Locate and identify every blood parasite.
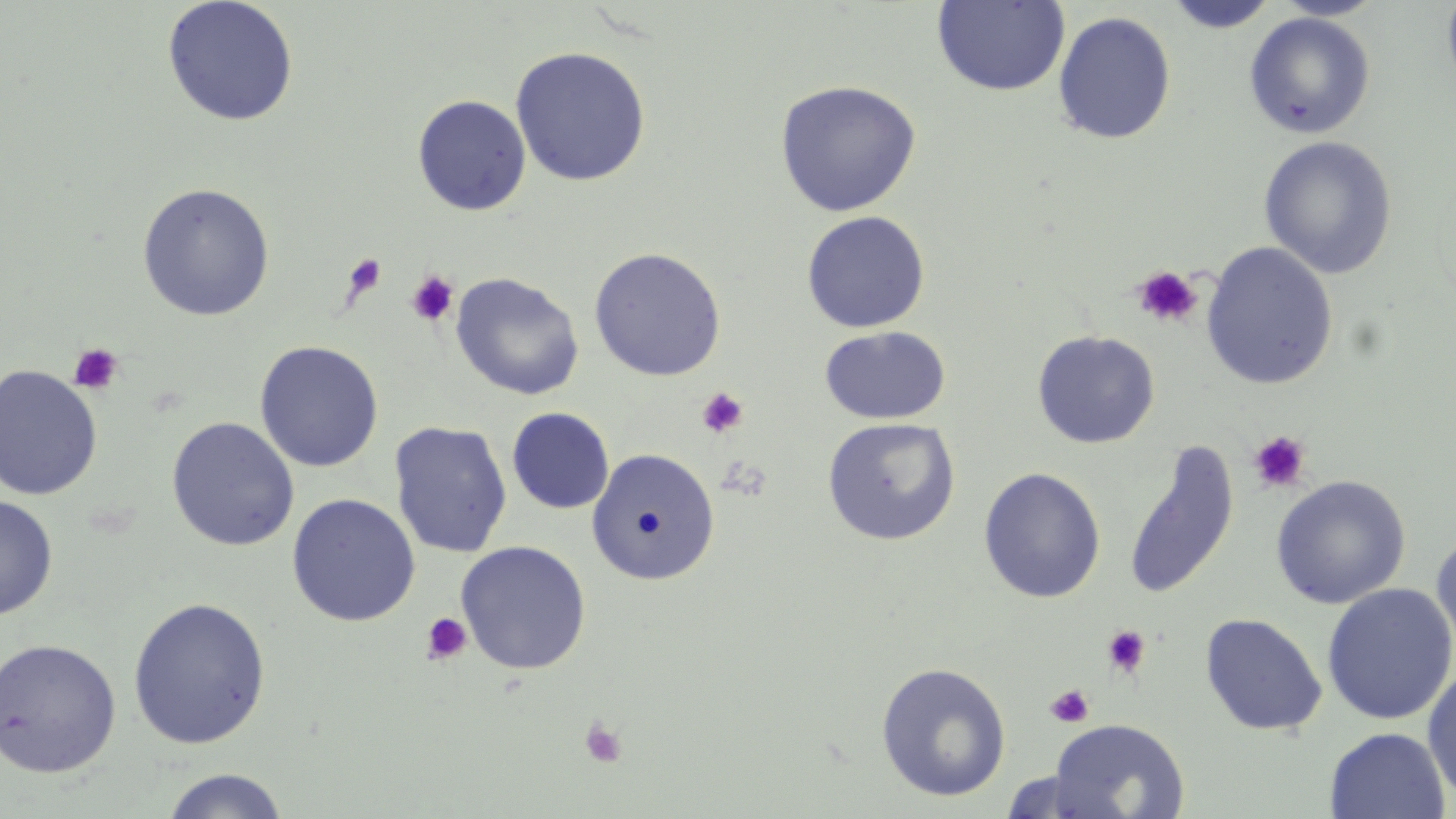
No blood parasites observed.

slide-level diagnosis = no evidence of blood parasites
image size = 1456×819 pixels
magnification = 1000x
field of view = single
platelet locations = approximate bounding boxes as named x1/y1/x2/y2 corners in pixels: (x1=342, y1=254, x2=388, y2=300), (x1=1132, y1=265, x2=1202, y2=328), (x1=406, y1=270, x2=459, y2=327), (x1=68, y1=343, x2=124, y2=396), (x1=696, y1=386, x2=749, y2=439), (x1=1249, y1=431, x2=1311, y2=493), (x1=420, y1=611, x2=473, y2=665), (x1=1101, y1=625, x2=1151, y2=679), (x1=1045, y1=684, x2=1094, y2=728), (x1=578, y1=716, x2=628, y2=769)
uninfected red blood cell locations = approximate bounding boxes as named x1/y1/x2/y2 corners in pixels: (x1=162, y1=0, x2=300, y2=127), (x1=1272, y1=0, x2=1387, y2=20), (x1=1441, y1=0, x2=1456, y2=101), (x1=931, y1=1, x2=1070, y2=96), (x1=1163, y1=1, x2=1279, y2=33), (x1=1053, y1=11, x2=1176, y2=145), (x1=1244, y1=12, x2=1375, y2=139), (x1=510, y1=45, x2=651, y2=186), (x1=774, y1=80, x2=922, y2=217), (x1=412, y1=94, x2=532, y2=216), (x1=1258, y1=135, x2=1398, y2=279), (x1=136, y1=183, x2=275, y2=321), (x1=801, y1=210, x2=930, y2=334), (x1=1201, y1=241, x2=1339, y2=390), (x1=588, y1=247, x2=727, y2=381), (x1=450, y1=273, x2=584, y2=400), (x1=819, y1=326, x2=951, y2=424), (x1=1032, y1=330, x2=1160, y2=449), (x1=254, y1=340, x2=383, y2=472), (x1=0, y1=364, x2=103, y2=500), (x1=507, y1=407, x2=615, y2=513), (x1=166, y1=416, x2=301, y2=552), (x1=821, y1=417, x2=961, y2=546), (x1=389, y1=421, x2=513, y2=558), (x1=1123, y1=441, x2=1240, y2=602), (x1=585, y1=447, x2=723, y2=582), (x1=978, y1=467, x2=1106, y2=603), (x1=1271, y1=475, x2=1411, y2=609), (x1=286, y1=493, x2=420, y2=626), (x1=0, y1=495, x2=58, y2=620), (x1=1430, y1=525, x2=1456, y2=658), (x1=455, y1=541, x2=592, y2=674), (x1=1321, y1=583, x2=1456, y2=725), (x1=128, y1=596, x2=271, y2=749), (x1=1200, y1=613, x2=1327, y2=736), (x1=0, y1=638, x2=122, y2=779), (x1=875, y1=661, x2=1011, y2=802), (x1=1422, y1=661, x2=1456, y2=805), (x1=1047, y1=717, x2=1190, y2=819), (x1=1324, y1=727, x2=1451, y2=819), (x1=159, y1=768, x2=291, y2=818)
stain = May-Grünwald-Giemsa
preparation = thin blood smear
modality = light microscopy